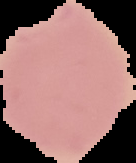 From a thin blood film. The area outside the segmented cell region is set to black. Malaria status: parasitized. Image is 136×163 pixels.